State which cell type is depicted.
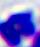
A leukocyte.

Summary:
  - Magnification: 400x
  - Modality: photomicrograph